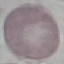

Summary:
  - Result: no malaria parasites detected
  - Stain: Giemsa
  - Image type: automatically extracted cell patch, resized to 64 × 64 pixels
  - Capture: smartphone through the microscope eyepiece
  - Preparation: thin blood smear